Locate every Plasmodium parasite.
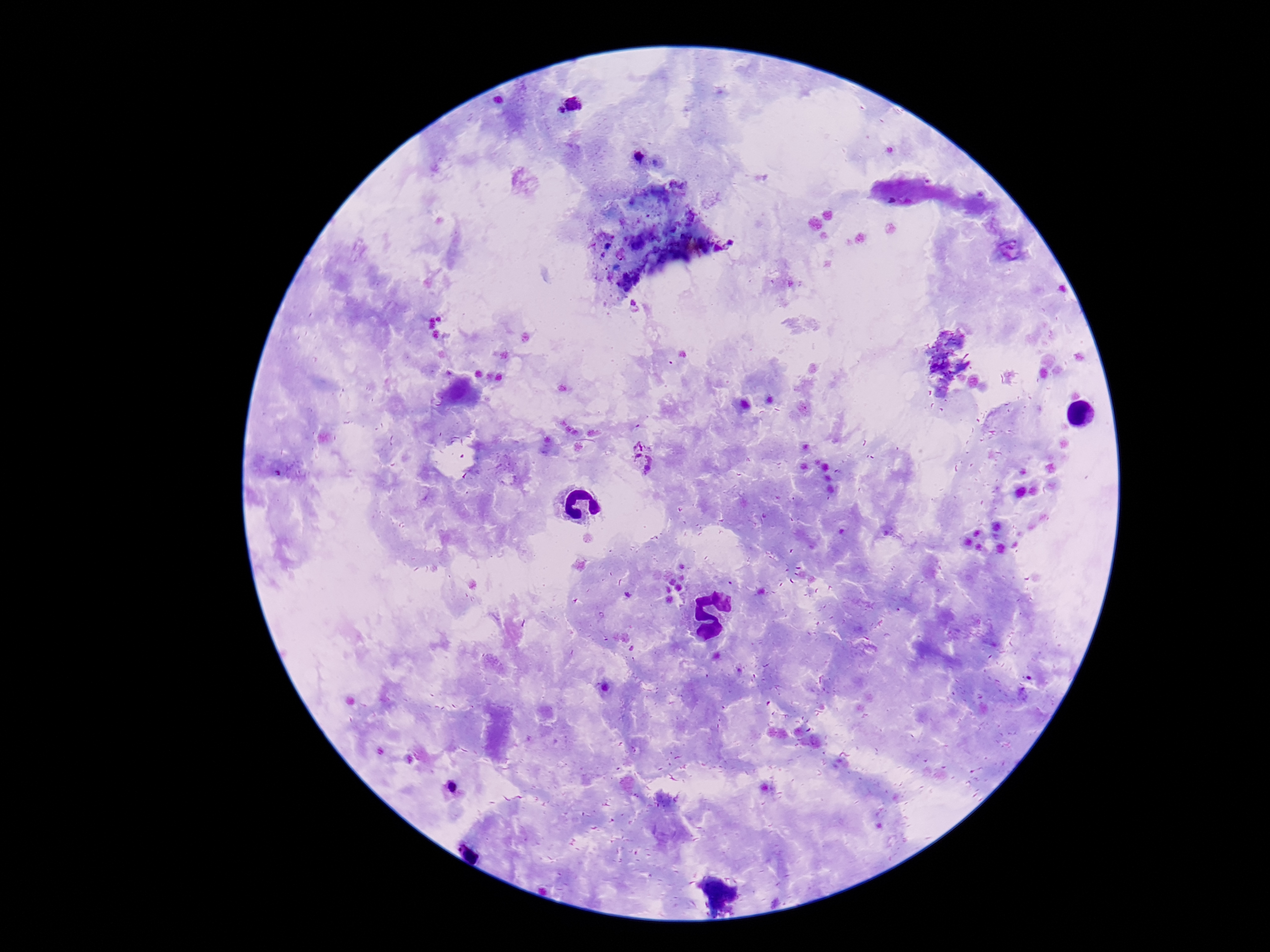
Approximate centers as [x, y] in pixels.
Plasmodium parasites: [575, 102], [559, 112], [638, 159], [642, 458], [450, 788].

{
  "image_size": "1270×952 pixels",
  "magnification": "100x",
  "patient_malaria_status": "infected",
  "field_of_view": "one from this slide",
  "capture": "smartphone camera through the microscope eyepiece",
  "preparation": "thick blood film",
  "stain": "Giemsa"
}